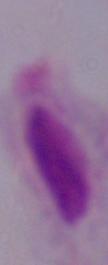 A trichomonad is shown. Captured at 1000x magnification. Micrograph.